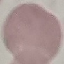

result = no malaria parasites seen
preparation = thin blood smear
stain = Giemsa
image type = automatically extracted cell patch, resized to 64 × 64 pixels
capture = smartphone camera at the microscope eyepiece